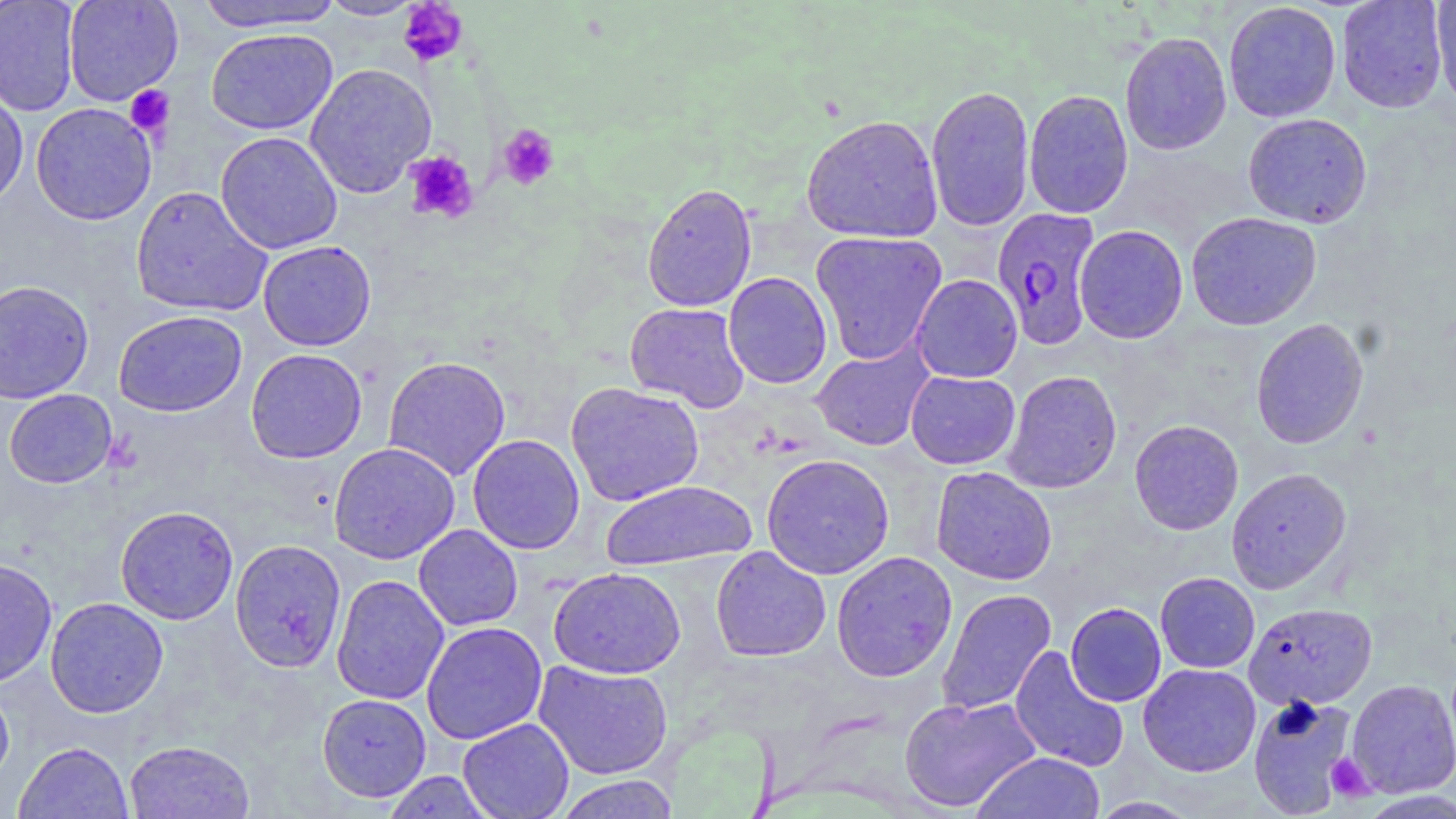
{
  "slide_level_diagnosis": "Plasmodium falciparum",
  "magnification": "1000x",
  "modality": "optical microscopy",
  "stain": "May-Grünwald-Giemsa",
  "field_of_view": "one of a larger specimen",
  "plasmodium_falciparum_infected_red_blood_cell_locations": "approximate bounding boxes as [x1, y1, x2, y2] in pixels: [991, 207, 1101, 350]",
  "image_size": "1456×819 pixels",
  "platelet_locations": "approximate bounding boxes as [x1, y1, x2, y2] in pixels: [399, 0, 469, 67], [125, 85, 175, 139], [497, 124, 560, 191], [404, 151, 479, 224], [1324, 753, 1375, 802]",
  "preparation": "thin blood film",
  "uninfected_red_blood_cell_locations": "approximate bounding boxes as [x1, y1, x2, y2] in pixels: [0, 0, 80, 116], [63, 0, 183, 106], [195, 0, 346, 33], [317, 0, 427, 21], [1336, 1, 1449, 113], [1431, 1, 1456, 110], [1223, 2, 1342, 123], [206, 28, 338, 135], [1119, 31, 1232, 156], [304, 63, 436, 198], [0, 83, 29, 210], [925, 84, 1035, 232], [1023, 89, 1133, 219], [30, 102, 157, 225], [1242, 112, 1372, 229], [800, 114, 943, 243], [216, 131, 343, 254], [642, 182, 758, 313], [130, 186, 272, 318], [1186, 211, 1322, 331], [1074, 225, 1188, 344], [810, 230, 948, 365], [258, 240, 376, 351], [723, 272, 832, 389], [911, 274, 1023, 383], [0, 279, 95, 404], [624, 302, 750, 412], [114, 310, 247, 417], [1250, 318, 1369, 449], [811, 342, 934, 452], [245, 348, 367, 463], [383, 356, 511, 481], [1002, 370, 1122, 494], [905, 371, 1020, 469], [566, 382, 704, 507], [4, 388, 118, 488], [1129, 419, 1244, 535], [467, 434, 585, 554], [328, 442, 460, 564], [761, 453, 894, 579], [931, 466, 1058, 586], [1226, 467, 1351, 594], [600, 480, 756, 570], [115, 505, 239, 625], [414, 524, 523, 631], [230, 539, 347, 673], [710, 546, 831, 662], [831, 551, 957, 682], [0, 558, 58, 687], [549, 567, 686, 679], [1155, 572, 1260, 673], [331, 574, 450, 706], [936, 588, 1056, 717], [45, 597, 168, 717], [1065, 602, 1166, 706], [1243, 602, 1377, 710], [421, 621, 548, 744], [1009, 646, 1129, 772], [533, 660, 673, 780], [1138, 664, 1261, 777], [0, 679, 14, 789], [1346, 679, 1456, 798], [317, 693, 432, 802], [900, 695, 1040, 812], [1247, 695, 1358, 817], [458, 718, 574, 819], [124, 740, 254, 818], [13, 741, 134, 818], [972, 752, 1105, 819], [381, 771, 495, 818], [553, 775, 679, 818], [1087, 796, 1205, 818]"
}